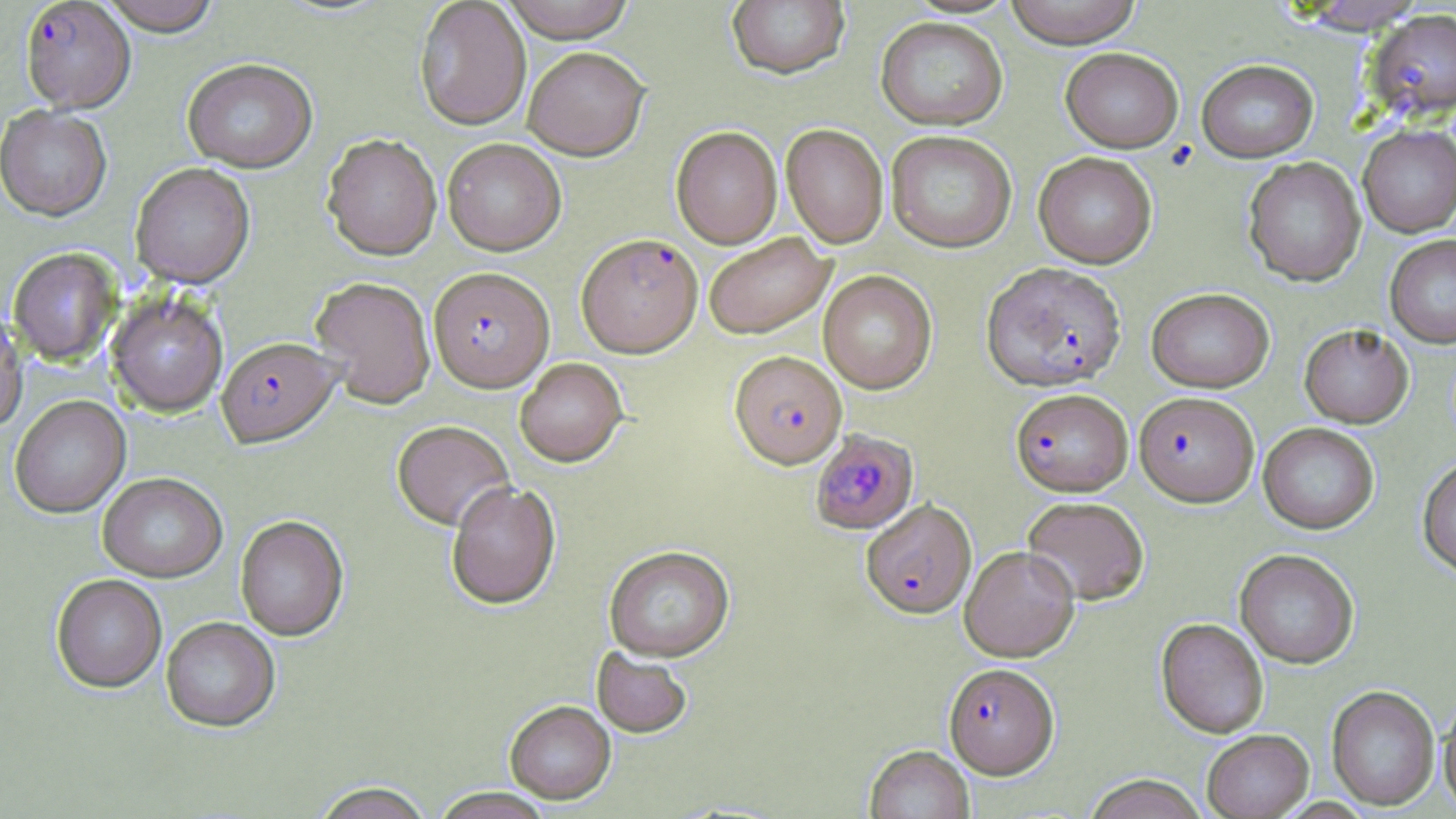

slide-level diagnosis = Plasmodium falciparum
image size = 1456×819 pixels
preparation = thin blood smear
stain = May-Grünwald-Giemsa
field of view = one of a larger specimen
Plasmodium falciparum-infected red blood cell locations = approximate bounding boxes as [x1, y1, x2, y2] in pixels: [20, 1, 136, 115], [1366, 9, 1456, 122], [576, 235, 703, 358], [981, 262, 1126, 392], [428, 268, 554, 394], [216, 338, 341, 450], [729, 351, 846, 469], [1010, 388, 1133, 496], [1138, 394, 1263, 509], [810, 429, 919, 535], [861, 499, 977, 620], [944, 663, 1059, 778]
modality = optical microscopy
magnification = 1000x
uninfected red blood cell locations = approximate bounding boxes as [x1, y1, x2, y2] in pixels: [97, 0, 222, 38], [498, 0, 637, 43], [726, 0, 850, 80], [1003, 0, 1143, 48], [414, 1, 531, 132], [1288, 1, 1430, 33], [876, 17, 1008, 130], [1060, 47, 1183, 153], [523, 48, 650, 162], [1197, 59, 1318, 162], [182, 61, 318, 174], [0, 107, 112, 224], [781, 124, 888, 248], [1358, 124, 1456, 237], [671, 127, 782, 249], [886, 131, 1017, 252], [322, 135, 442, 262], [442, 139, 566, 256], [1034, 152, 1157, 268], [1243, 157, 1366, 286], [130, 164, 255, 289], [704, 233, 834, 340], [1385, 234, 1456, 347], [8, 249, 121, 367], [819, 270, 937, 394], [310, 277, 437, 409], [1146, 287, 1274, 392], [106, 291, 228, 417], [0, 314, 28, 435], [1299, 323, 1413, 428], [515, 358, 627, 468], [10, 397, 131, 520], [391, 422, 514, 532], [1258, 422, 1380, 534], [1417, 457, 1456, 578], [98, 475, 227, 584], [446, 483, 561, 611], [1022, 496, 1150, 605], [236, 517, 349, 642], [960, 546, 1079, 661], [604, 548, 735, 663], [1235, 549, 1359, 668], [51, 576, 167, 694], [161, 618, 280, 733], [1156, 618, 1269, 737], [591, 649, 692, 739], [1327, 684, 1439, 810], [1438, 694, 1456, 815], [505, 703, 616, 806], [1202, 729, 1313, 818], [865, 745, 974, 819], [1082, 774, 1208, 819], [311, 782, 436, 819], [432, 788, 553, 819]